Assess this cell for malaria.
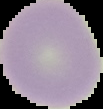

It is uninfected.

The area outside the segmented cell region is set to black. Image is 103×109 pixels. From a thin blood film.